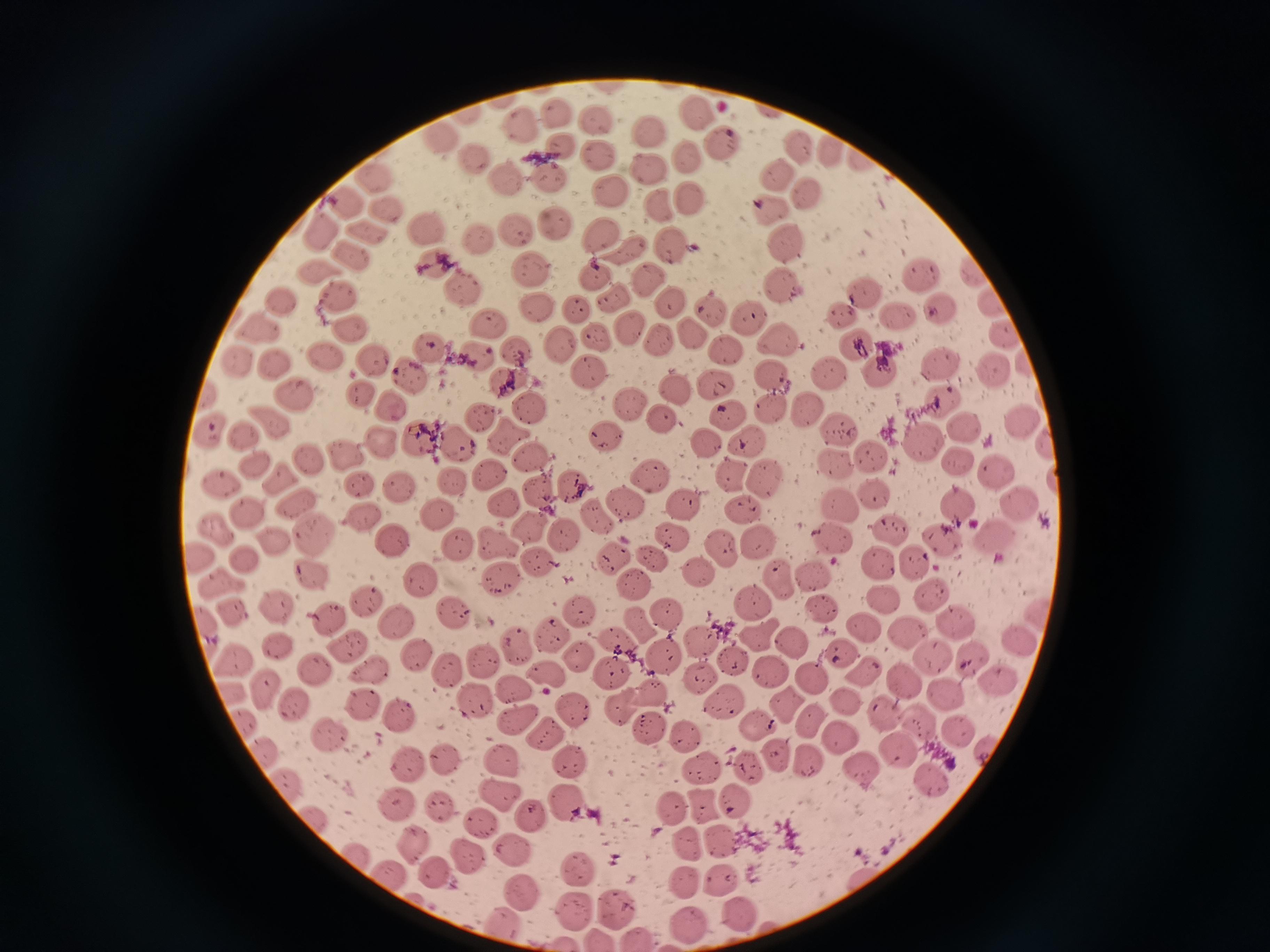
Approximate centers as (x, y) in pixels. Cell locations: (698, 112), (466, 115), (558, 115), (596, 115), (524, 125), (650, 131), (440, 136), (796, 141), (720, 143), (563, 147), (833, 153), (600, 155), (687, 156), (473, 157), (646, 169), (507, 176), (774, 177), (550, 179), (369, 181), (609, 192), (806, 193), (689, 199), (342, 203), (659, 208), (767, 208), (390, 212), (556, 226), (322, 228), (370, 229), (516, 229), (429, 230), (600, 233), (480, 239), (673, 245), (789, 245), (624, 247), (354, 256), (434, 263), (532, 269), (317, 270), (919, 271), (973, 274), (599, 276), (648, 278), (462, 286), (783, 286), (860, 289), (339, 295), (612, 300), (279, 301), (990, 302), (669, 306), (535, 308), (573, 308), (709, 309), (941, 311), (840, 312), (899, 315), (749, 317), (489, 324), (259, 327), (629, 327), (352, 329), (691, 332), (1002, 335), (596, 336), (659, 342), (780, 343), (558, 344), (427, 345), (858, 345), (730, 351), (517, 352), (479, 355), (326, 357), (371, 357), (236, 359), (276, 364), (941, 365), (989, 369), (588, 372), (831, 374), (880, 374), (772, 376), (411, 377), (509, 382), (716, 385), (675, 389), (359, 392), (207, 393), (296, 394), (939, 402), (628, 403), (393, 405), (531, 407), (805, 408), (773, 411), (728, 414), (485, 415), (662, 417), (1024, 419), (269, 420), (963, 428), (211, 430), (836, 430), (243, 432), (509, 436), (418, 438), (608, 438), (920, 438), (744, 441), (704, 442), (378, 443), (460, 444), (1046, 445), (345, 454), (307, 458), (532, 460), (869, 460), (254, 461), (957, 462), (829, 464), (996, 470), (732, 473), (485, 475), (281, 477), (647, 477), (766, 477), (450, 482), (219, 483), (357, 483), (572, 486), (401, 488), (539, 493), (874, 496), (505, 502), (685, 502), (626, 503), (960, 503), (296, 504), (837, 506), (1023, 506), (245, 510), (740, 512), (365, 515), (438, 515), (594, 519), (531, 528), (217, 530), (891, 531), (673, 535), (318, 536), (565, 536), (944, 538), (997, 538), (272, 540), (392, 540), (837, 540), (498, 543), (757, 544), (456, 546), (720, 549), (197, 554), (655, 557), (242, 558), (613, 558), (914, 558), (538, 561), (881, 566), (695, 571), (310, 572), (814, 574), (218, 581), (422, 581), (500, 581), (778, 581), (634, 586), (931, 596), (882, 599), (366, 601), (751, 604), (275, 606), (825, 608), (578, 609), (234, 610), (1037, 610), (326, 614), (453, 615), (669, 617), (395, 621), (864, 625), (957, 625), (638, 627), (907, 630), (553, 633), (207, 635), (754, 636), (615, 638), (702, 638), (1016, 638), (792, 640), (277, 644), (515, 645), (346, 647), (842, 651), (666, 653), (415, 654), (583, 654), (234, 659), (733, 659), (933, 659), (971, 659), (480, 661), (315, 670), (370, 670), (611, 670), (771, 670), (865, 671), (448, 672), (699, 673), (550, 676), (812, 679), (1000, 679), (904, 680), (265, 689), (514, 689), (648, 690), (229, 695), (945, 698), (473, 702), (845, 702), (786, 703), (293, 704), (360, 705), (720, 705), (575, 706), (620, 713), (884, 715), (397, 717), (918, 719), (811, 720), (243, 721), (516, 723), (759, 725), (649, 728), (960, 730), (547, 735), (685, 735), (327, 737), (843, 737), (897, 749), (985, 751), (263, 752), (775, 754), (441, 759), (504, 761), (807, 761), (572, 762), (409, 765), (750, 767), (698, 768), (857, 772), (932, 784), (285, 785), (495, 792), (739, 801), (396, 803), (569, 803), (702, 804), (441, 808), (670, 809), (529, 816), (308, 817), (482, 822), (718, 841), (688, 843), (411, 845), (511, 851), (356, 853), (462, 854), (576, 873), (435, 874), (393, 877), (722, 879), (684, 883), (521, 893), (572, 908), (620, 910), (741, 916), (506, 925), (689, 928), (633, 937), (599, 939), (567, 943). Image is 1270×952 pixels. Acquired by smartphone through the microscope eyepiece. Thin blood smear. Giemsa stain. Single field of view.